Outline each blood parasite and name the species.
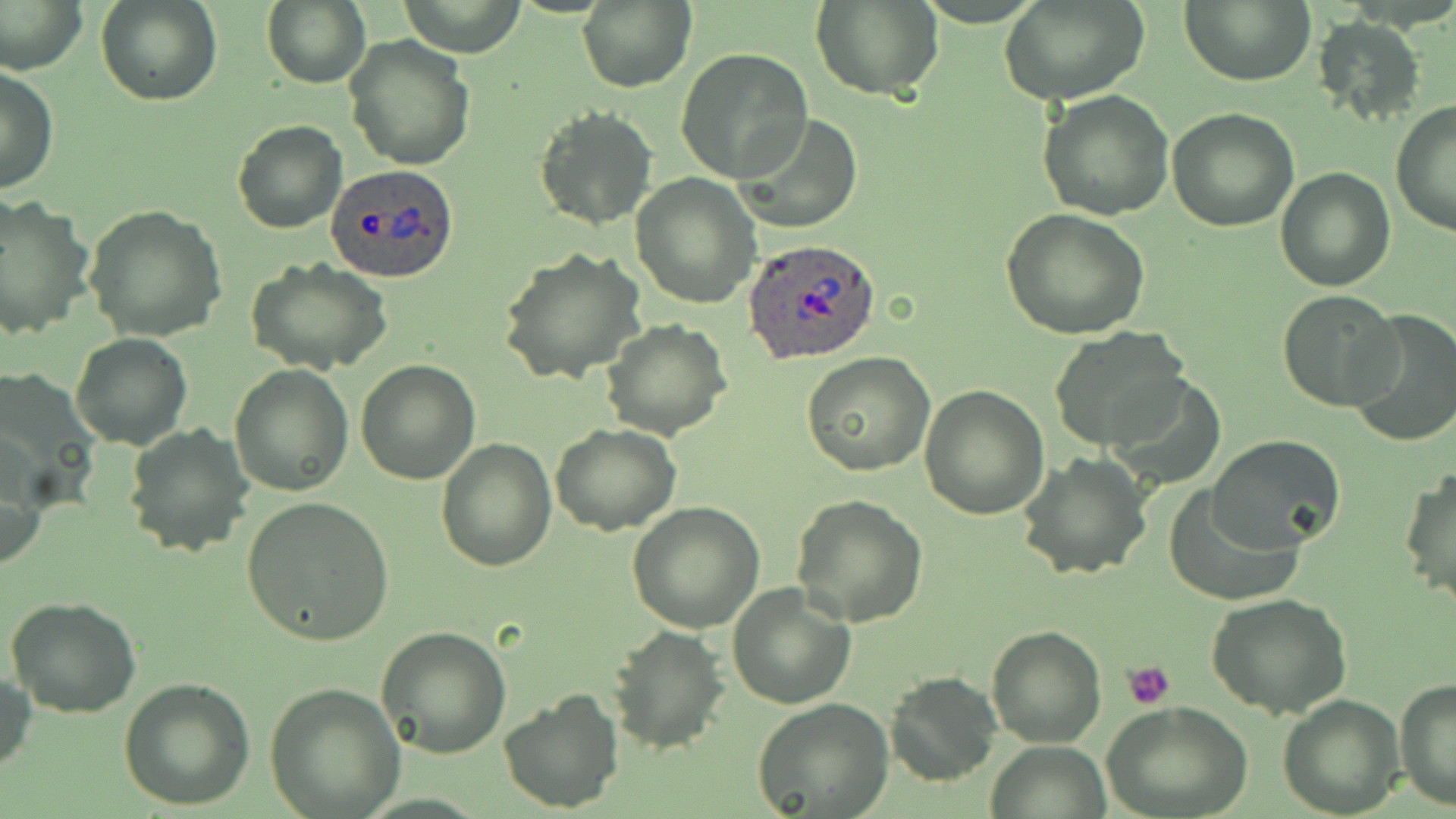
Approximate bounding boxes as (x1, y1, x2, y2) in pixels.
Plasmodium ovale-infected red blood cells: (326, 164, 462, 283), (743, 239, 881, 366).
No Plasmodium falciparum, Plasmodium malariae, Plasmodium vivax, Babesia divergens, or Trypanosoma brucei observed.

Summary:
  - Platelet locations: (1122, 661, 1176, 710)
  - Uninfected red blood cell locations: (96, 0, 221, 106), (1180, 0, 1316, 85), (1, 1, 87, 74), (262, 1, 372, 90), (395, 1, 527, 57), (576, 1, 696, 91), (810, 1, 943, 100), (1001, 1, 1147, 105), (1313, 14, 1425, 122), (344, 36, 476, 174), (676, 49, 813, 182), (0, 65, 59, 194), (1038, 90, 1174, 221), (1390, 100, 1456, 238), (533, 104, 657, 231), (1166, 108, 1299, 230), (734, 113, 864, 234), (232, 119, 346, 234), (1275, 166, 1396, 293), (631, 174, 762, 308), (0, 196, 93, 340), (82, 205, 227, 342), (999, 208, 1151, 340), (499, 248, 646, 386), (247, 257, 392, 375), (1276, 289, 1401, 412), (1345, 309, 1456, 447), (601, 319, 732, 441), (1047, 328, 1190, 451), (69, 332, 193, 450), (803, 353, 935, 478), (355, 359, 481, 484), (228, 364, 354, 496), (1103, 370, 1226, 489), (919, 384, 1049, 520), (549, 423, 679, 535), (123, 424, 253, 557), (1207, 434, 1347, 552), (1, 436, 45, 572), (436, 438, 557, 572), (1017, 451, 1152, 582), (1401, 464, 1455, 606), (1163, 492, 1302, 605), (791, 494, 929, 627), (241, 497, 394, 645), (627, 501, 767, 632), (727, 583, 857, 710), (1207, 594, 1352, 720), (6, 597, 141, 717), (608, 624, 729, 752), (378, 625, 511, 758), (986, 626, 1108, 747), (0, 669, 36, 780), (883, 671, 1000, 788), (1395, 676, 1455, 812), (119, 677, 254, 811), (264, 683, 405, 818), (497, 685, 624, 814), (1276, 693, 1404, 817), (752, 696, 894, 817), (1102, 700, 1253, 819), (989, 740, 1111, 818)
  - Slide-level diagnosis: Plasmodium ovale
  - Stain: May-Grünwald-Giemsa
  - Modality: light microscopy
  - Preparation: thin blood smear
  - Image size: 1456×819 pixels
  - Magnification: 1000x
  - Field of view: one of a larger specimen